Classify this cell by malaria status.
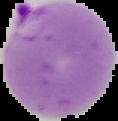
It is parasitized.

The area outside the segmented cell region is set to black. Image is 118×121 pixels. From a thin blood film.